Report the malaria status of this cell.
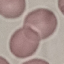
Uninfected.

Summary:
  - Stain: Giemsa
  - Preparation: thin blood film
  - Image type: automatically extracted cell patch, resized to 64 × 64 pixels
  - Capture: smartphone through the microscope eyepiece